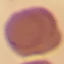

result = no malaria parasites detected
preparation = thin smear
image type = cell patch, automatically extracted from a larger field of view and resized to 64 × 64 pixels
capture = smartphone through the microscope eyepiece
stain = Giemsa